Name the parasite shown.
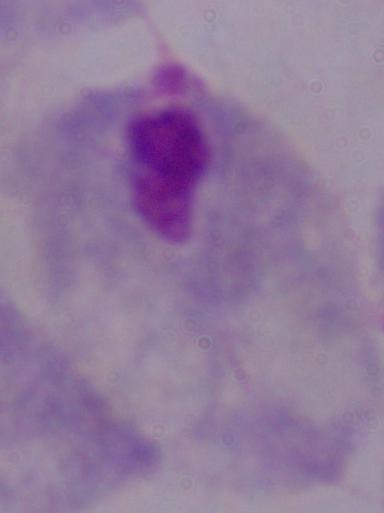
A trichomonad.

modality: photomicrograph
magnification: 1000x